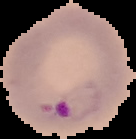

From a thin blood film. Malaria status: parasitized. The area outside the segmented cell region is set to black. Image is 136×139 pixels.